Assess the morphology of the red blood cells.
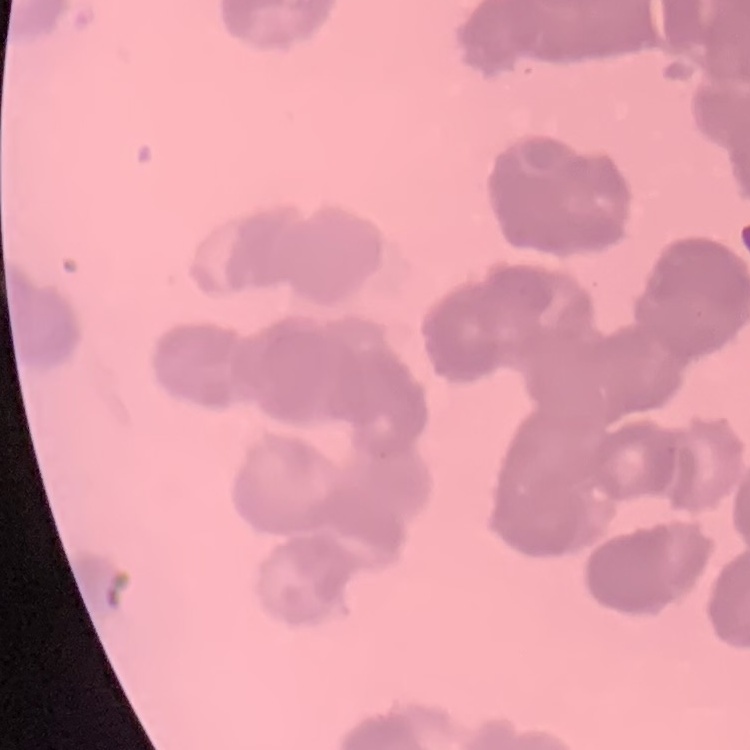
They show rouleaux formation.

Square crop of a larger photomicrograph. Field's or Giemsa stain. Thin peripheral smear.